Name the parasite shown.
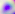

This is Toxoplasma gondii.

modality: micrograph
magnification: 400x